Point out each malaria parasite.
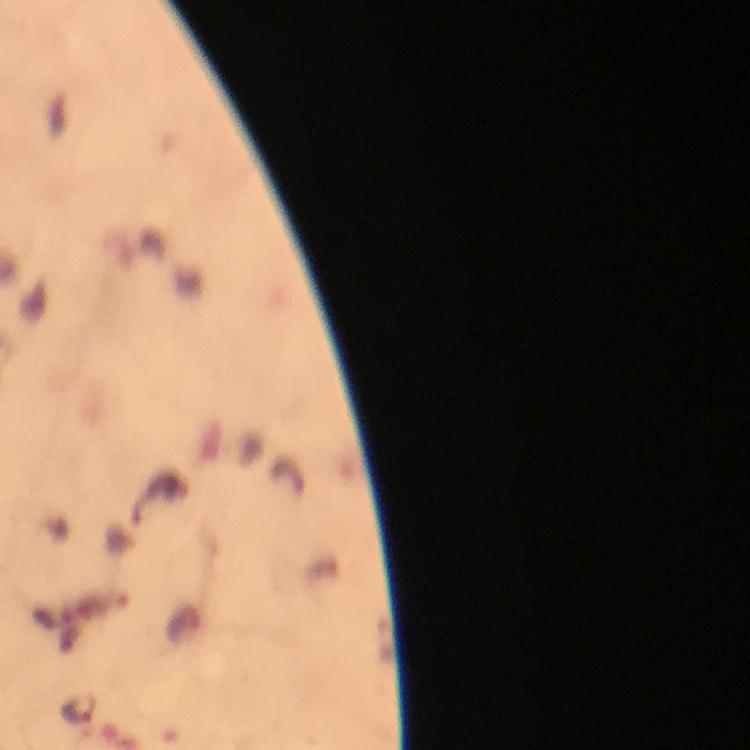

Approximate object centers, in pixels from the top-left corner.
Malaria parasites: (x=78, y=711).

Summary:
  - Image size: 750×750 pixels
  - Stain: Giemsa
  - Cropped from: one field of view
  - Context: from a malaria diagnostic workup
  - Capture: smartphone mounted on the microscope
  - Immersion oil: applied
  - Preparation: thick blood smear
  - Magnification: 100x